Look for Plasmodium parasites.
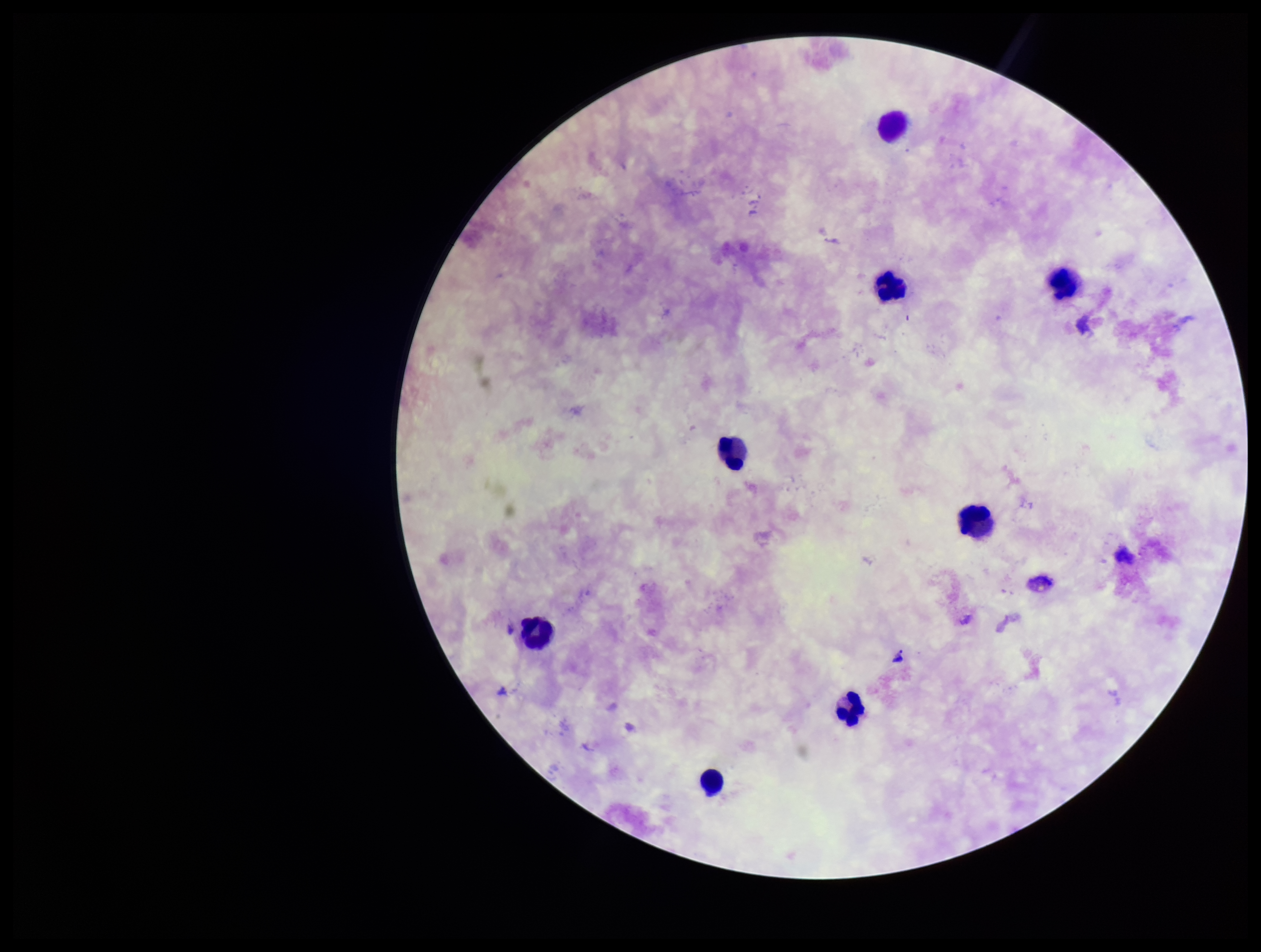
None identified.

Stained with Giemsa. Patient malaria status: negative. Image is 1261×952 pixels. Leukocyte count: 8. Photographed through the microscope eyepiece with a smartphone camera. Parasite count: 0. Single field of view. Preparation: thick.